Name the parasite shown.
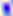
This is Toxoplasma gondii.

modality: photomicrograph
magnification: 400x